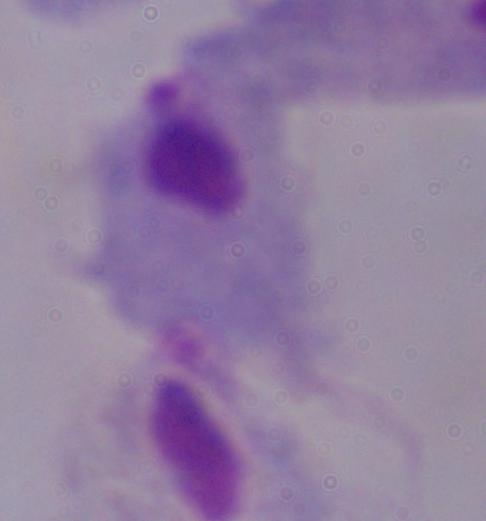
identification = trichomonad
modality = photomicrograph
magnification = 1000x